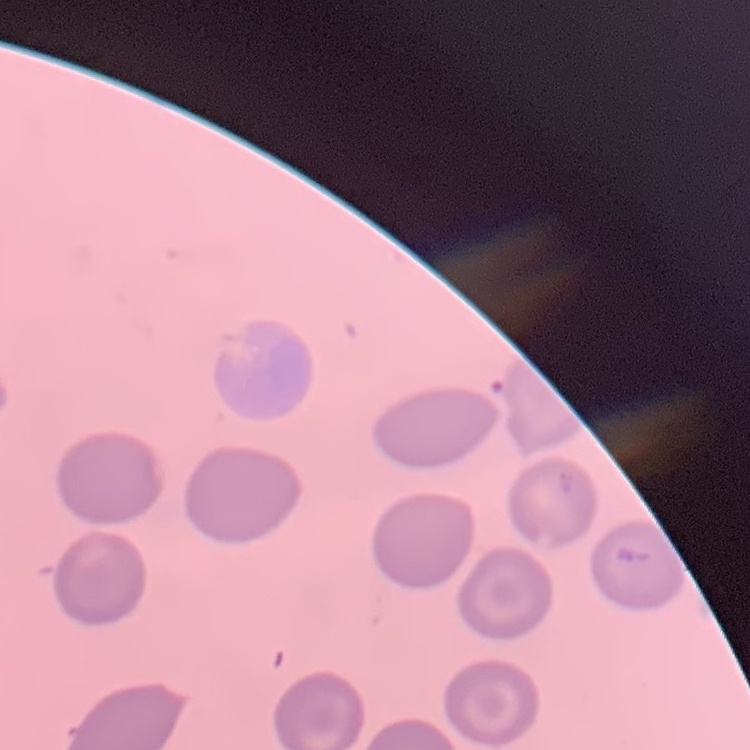

The red blood cells exhibit no rouleaux formation. One tile cut from a larger photomicrograph. Field's or Giemsa stain. Thin peripheral smear.